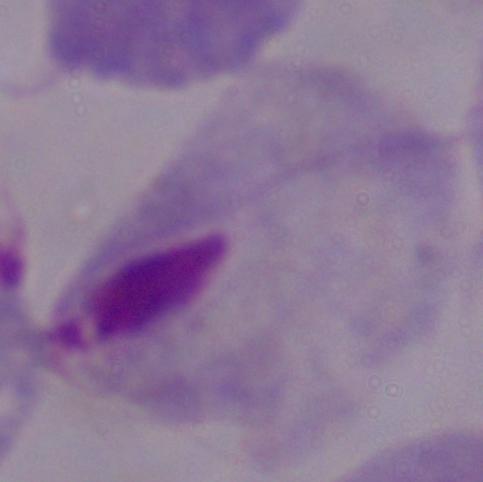

{
  "modality": "photomicrograph",
  "magnification": "1000x",
  "identification": "trichomonad"
}